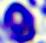 Micrograph. 400x magnification. A leukocyte is shown.